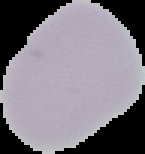

Summary:
  - Preparation: thin blood film
  - Image size: 145×154 pixels
  - Image type: segmented cell region with the area outside set to black
  - Malaria status: uninfected